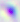
identification = Toxoplasma gondii
modality = micrograph
magnification = 400x